State which cell type is depicted.
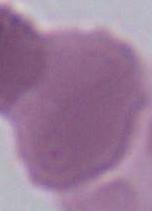

This is an erythrocyte.

modality = photomicrograph
magnification = 1000x